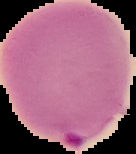 Image is 136×154 pixels. From a thin blood film. Malaria status: parasitized. The area outside the segmented cell region is set to black.